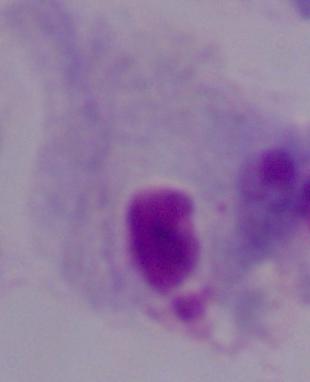

Summary:
  - Magnification: 1000x
  - Modality: photomicrograph
  - Identification: trichomonad